Give the extent of all uninfected red blood cells.
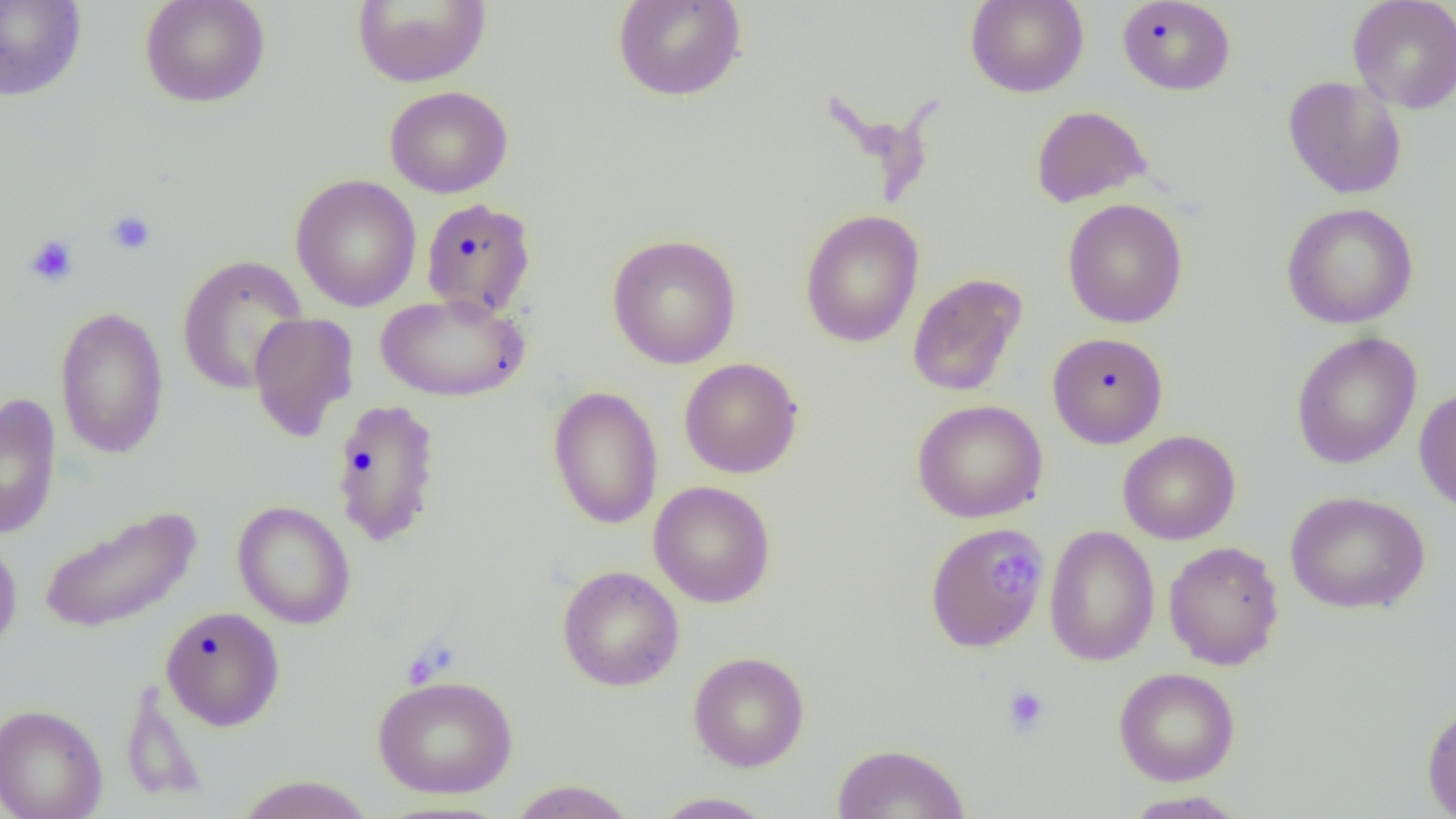

Approximate bounding boxes as [x1, y1, x2, y2] in pixels.
Uninfected red blood cells: [0, 0, 88, 102], [139, 0, 271, 108], [352, 0, 491, 88], [612, 0, 747, 102], [965, 0, 1089, 98], [1347, 0, 1456, 114], [1116, 1, 1236, 96], [1282, 76, 1407, 200], [384, 85, 514, 198], [1030, 105, 1151, 208], [290, 174, 422, 312], [420, 198, 537, 318], [1062, 198, 1188, 329], [1281, 202, 1419, 329], [800, 210, 924, 348], [605, 232, 742, 369], [175, 254, 310, 395], [907, 273, 1026, 398], [375, 292, 529, 403], [54, 305, 170, 460], [247, 312, 359, 442], [1047, 332, 1168, 449], [1290, 332, 1422, 469], [679, 358, 803, 478], [547, 386, 664, 529], [1413, 386, 1456, 514], [0, 393, 62, 541], [330, 398, 442, 547], [912, 399, 1048, 523], [1117, 430, 1241, 545], [649, 480, 776, 608], [1285, 491, 1430, 614], [232, 501, 356, 629], [38, 505, 201, 634], [923, 521, 1049, 653], [1044, 524, 1160, 666], [0, 536, 23, 658], [1163, 540, 1284, 670], [557, 565, 684, 691], [160, 606, 286, 730], [688, 651, 810, 772], [1113, 667, 1240, 786], [371, 674, 519, 799], [119, 681, 209, 805], [0, 703, 108, 819], [1421, 703, 1456, 818], [832, 742, 971, 819], [235, 774, 376, 818], [507, 779, 639, 819], [1122, 790, 1248, 818], [649, 791, 779, 818].

Platelet locations: [105, 210, 156, 256], [25, 235, 79, 287], [999, 549, 1036, 594], [1002, 685, 1050, 737]. Slide-level diagnosis: no evidence of blood parasites. Thin blood film. 1000x magnification. Image is 1456×819 pixels. One field of a larger specimen. Light microscopy.